Assess this cell for malaria.
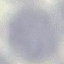

Uninfected.

Summary:
  - Stain: Giemsa
  - Image type: automatically extracted cell patch, resized to 64 × 64 pixels
  - Preparation: thin blood smear
  - Capture: smartphone camera at the microscope eyepiece